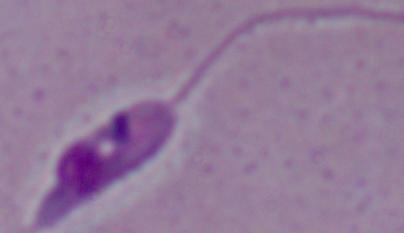

{
  "modality": "photomicrograph",
  "magnification": "1000x",
  "identification": "Leishmania"
}